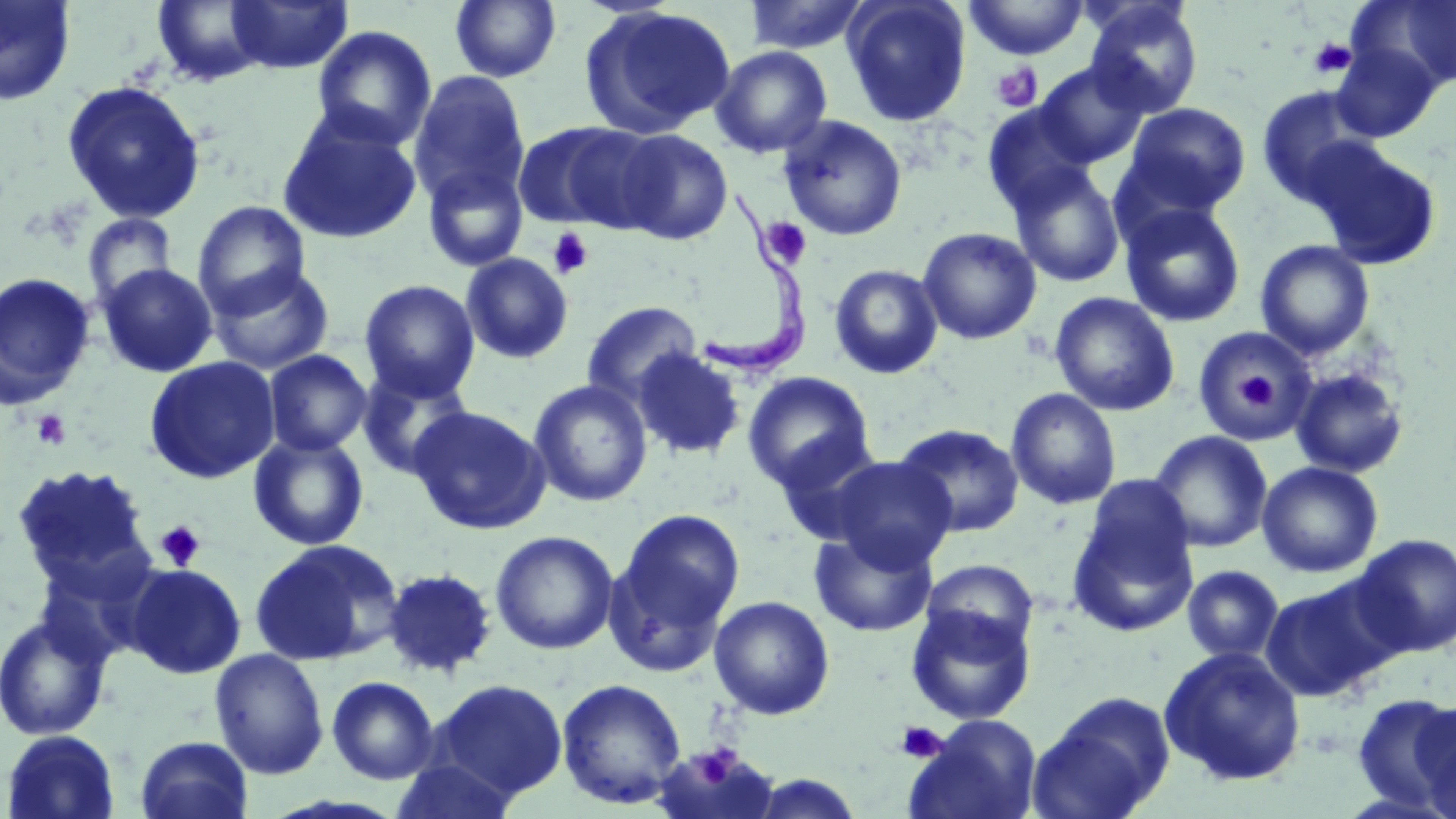 Approximate bounding boxes as [x1, y1, x2, y2] in pixels. Uninfected red blood cell locations: [0, 0, 77, 107], [150, 0, 272, 86], [225, 0, 353, 74], [743, 0, 870, 54], [842, 0, 971, 126], [964, 0, 1089, 60], [1346, 0, 1456, 93], [450, 1, 561, 83], [1082, 1, 1204, 117], [580, 5, 736, 140], [312, 24, 438, 150], [1330, 42, 1443, 142], [711, 45, 833, 159], [1033, 61, 1152, 167], [408, 71, 531, 210], [61, 80, 206, 224], [1255, 86, 1377, 206], [1122, 103, 1251, 217], [277, 110, 423, 245], [777, 115, 908, 241], [513, 121, 651, 232], [614, 128, 733, 245], [1303, 139, 1442, 271], [422, 162, 529, 273], [1007, 162, 1126, 288], [192, 201, 311, 317], [1119, 203, 1246, 328], [82, 214, 178, 311], [917, 226, 1042, 344], [1255, 240, 1375, 359], [460, 253, 574, 364], [98, 263, 218, 377], [829, 263, 943, 379], [208, 264, 335, 375], [0, 272, 96, 409], [359, 279, 480, 402], [1049, 292, 1179, 416], [582, 301, 703, 407], [1191, 326, 1317, 445], [632, 348, 746, 460], [263, 349, 372, 456], [144, 355, 280, 484], [1290, 366, 1410, 478], [357, 367, 474, 479], [742, 371, 876, 494], [528, 379, 653, 507], [1005, 388, 1122, 509], [409, 405, 550, 534], [894, 423, 1025, 538], [1149, 430, 1273, 553], [248, 432, 369, 551], [826, 455, 957, 571], [1257, 461, 1383, 577], [11, 463, 154, 589], [1080, 473, 1197, 582], [1068, 505, 1199, 636], [607, 509, 745, 671], [809, 528, 938, 638], [490, 530, 619, 655], [1351, 533, 1456, 658], [249, 539, 401, 667], [920, 558, 1039, 656], [125, 563, 247, 678], [1181, 565, 1283, 663], [381, 567, 498, 679], [1260, 579, 1395, 703], [708, 595, 835, 720], [906, 604, 1035, 724], [0, 614, 113, 740], [1159, 645, 1307, 786], [209, 648, 329, 780], [326, 675, 440, 785], [556, 678, 687, 809], [429, 679, 568, 802], [1029, 691, 1176, 818], [1351, 693, 1456, 812], [1413, 702, 1456, 819], [904, 715, 1043, 819], [1, 729, 122, 819], [134, 735, 254, 819], [390, 758, 523, 819], [746, 773, 867, 818]. Trypanosoma brucei locations: [697, 184, 814, 383]. Platelet locations: [1309, 38, 1356, 79], [991, 62, 1043, 112], [759, 217, 812, 269], [547, 228, 593, 279], [1237, 372, 1276, 410], [31, 409, 73, 450], [155, 521, 205, 570], [895, 720, 946, 763], [685, 743, 746, 787]. Slide-level diagnosis: Trypanosoma brucei. Captured at 1000x magnification. Image is 1456×819 pixels. Optical microscopy. Single field of view. Thin blood smear. May-Grünwald-Giemsa stain.